Report the malaria status of this cell.
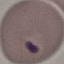
It is parasitized.

preparation: thin smear
capture: smartphone camera at the microscope eyepiece
stain: Giemsa
image_type: cell patch, automatically extracted from a larger field of view and resized to 64 × 64 pixels